Name the parasite shown.
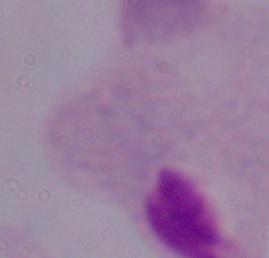
This is a trichomonad.

modality: micrograph
magnification: 1000x